Name the parasite shown.
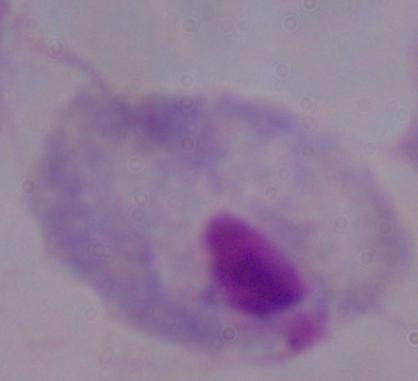

A trichomonad.

1000x magnification. Micrograph.